Evaluate for malaria.
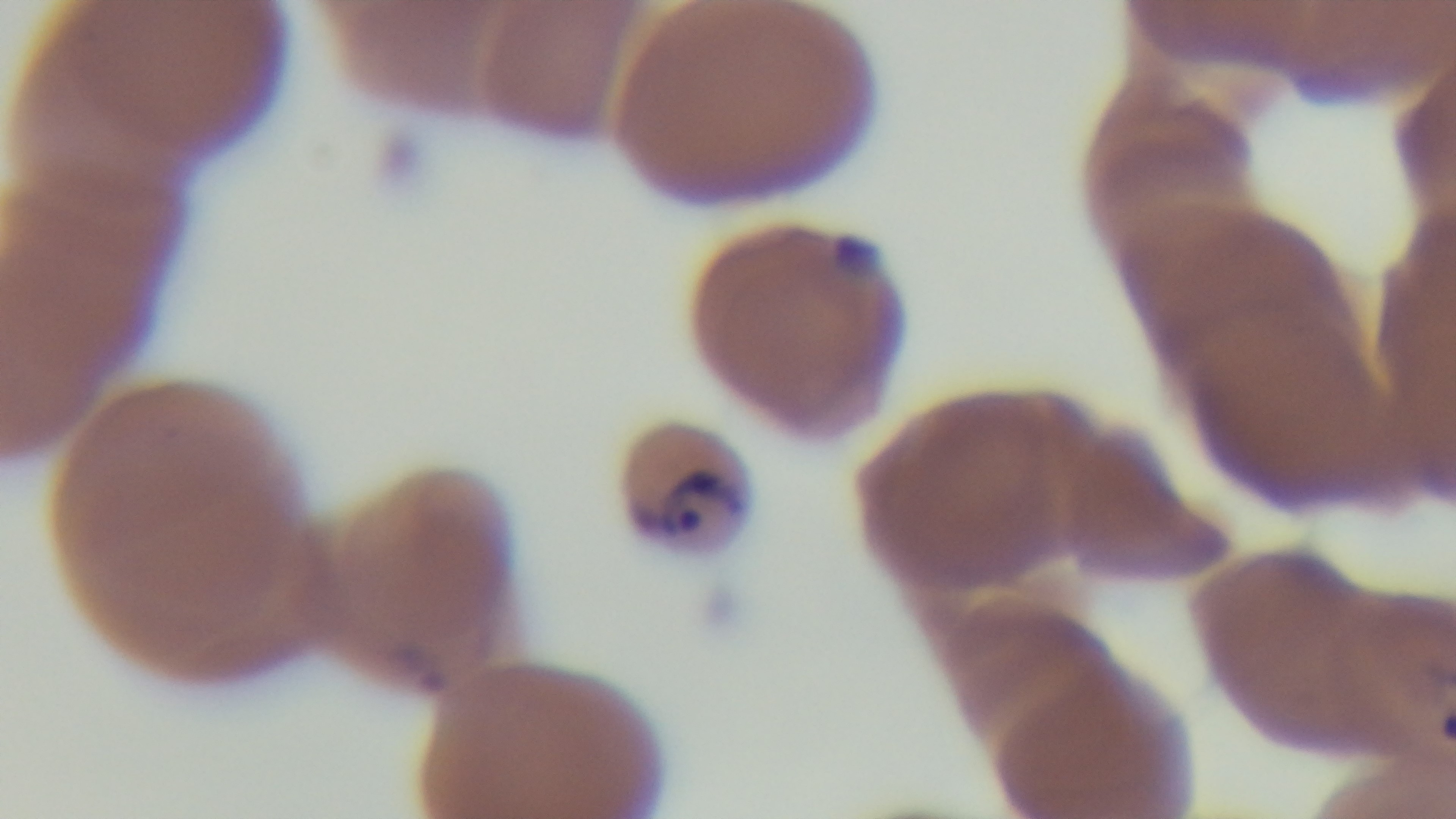

Infected.

field of view = single
capture = mounted 4K digital camera
objective = 100x oil immersion
preparation = thin smear
stain = Giemsa
modality = light microscopy